Name the blood parasite species.
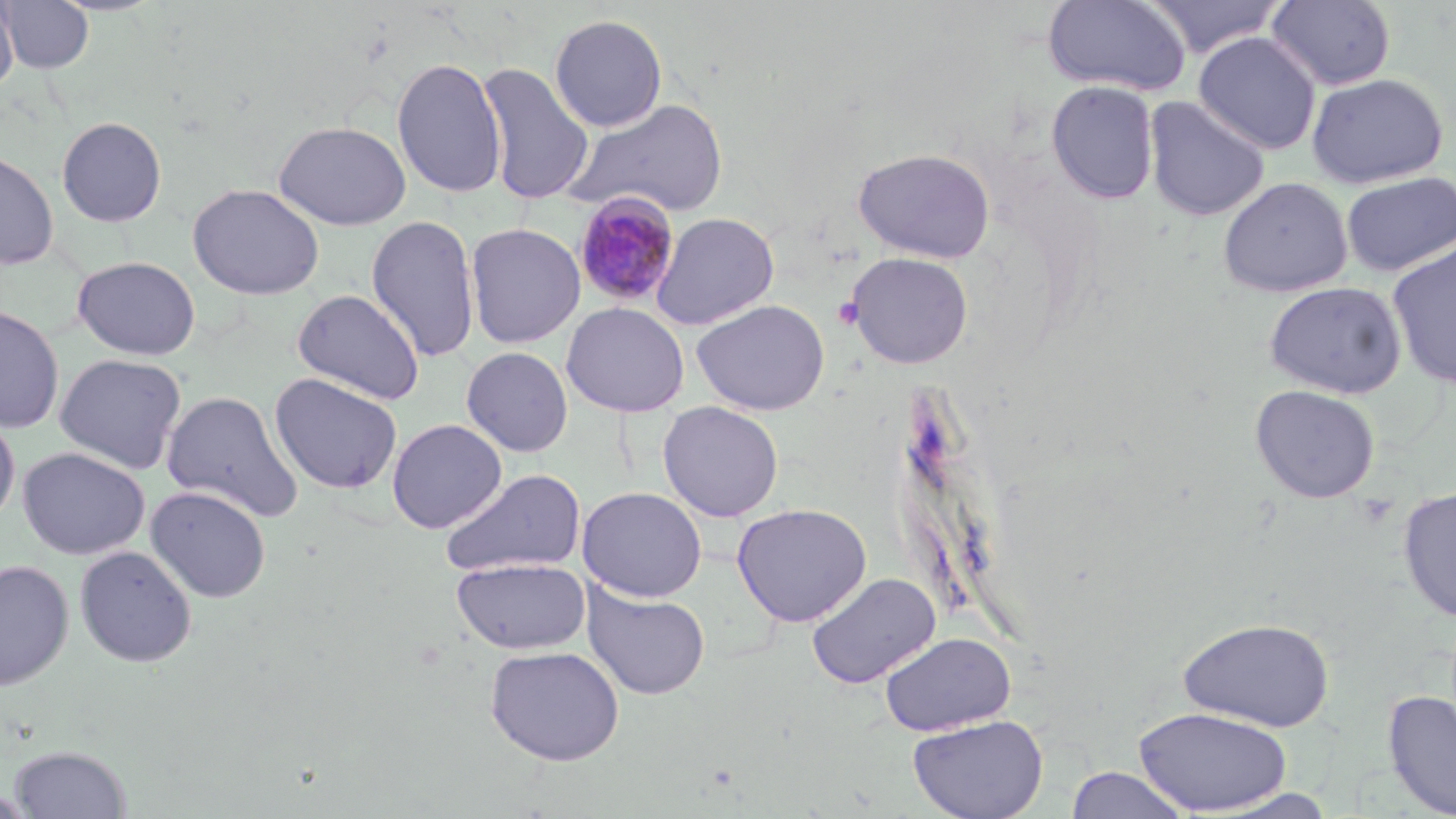

Plasmodium malariae.

{
  "preparation": "thin blood smear",
  "magnification": "1000x",
  "image_size": "1456×819 pixels",
  "field_of_view": "single",
  "uninfected_red_blood_cell_locations": "approximate bounding boxes as (x1,y1)-(x2,y2) corner pairs in pixels: (0,0)-(19,95), (1,0)-(94,73), (1144,0)-(1286,59), (1266,0)-(1397,91), (1043,1)-(1192,95), (549,14)-(668,132), (1193,32)-(1321,155), (391,56)-(507,199), (475,62)-(595,205), (1307,72)-(1448,188), (1047,81)-(1159,204), (1143,96)-(1271,221), (565,97)-(731,219), (56,116)-(167,227), (273,120)-(412,231), (853,147)-(995,263), (0,150)-(59,270), (1341,171)-(1455,276), (1217,177)-(1353,297), (187,183)-(325,300), (651,212)-(780,330), (365,214)-(480,363), (465,222)-(585,348), (1386,240)-(1456,390), (845,251)-(974,369), (72,256)-(201,360), (1264,281)-(1407,398), (292,288)-(425,405), (691,299)-(830,415), (561,302)-(689,417), (0,304)-(65,434), (461,346)-(574,457), (54,353)-(187,475), (269,372)-(403,494), (1249,384)-(1381,503), (161,390)-(303,523), (658,401)-(784,522), (0,409)-(20,527), (387,418)-(507,533), (17,447)-(150,559), (440,468)-(587,577), (146,485)-(271,602), (577,486)-(707,602), (1397,487)-(1456,622), (731,502)-(872,627), (74,545)-(197,667), (451,556)-(591,655), (0,560)-(74,691), (807,572)-(941,689), (581,582)-(711,701), (1178,617)-(1335,732), (878,631)-(1017,736), (484,645)-(625,765), (1383,689)-(1456,818), (1134,706)-(1293,815), (907,714)-(1049,819), (9,744)-(132,818), (1065,766)-(1191,818), (0,789)-(36,818)",
  "platelet_locations": "approximate bounding boxes as (x1,y1)-(x2,y2) corner pairs in pixels: (832,296)-(864,330), (1355,493)-(1400,529)",
  "plasmodium_malariae_infected_red_blood_cell_locations": "approximate bounding boxes as (x1,y1)-(x2,y2) corner pairs in pixels: (573,191)-(682,309)",
  "modality": "optical microscopy",
  "stain": "May-Grünwald-Giemsa"
}